Classify this cell by malaria status.
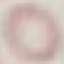
It is uninfected.

{
  "image_type": "cell patch, automatically extracted from a larger field of view and resized to 64 × 64 pixels",
  "stain": "Giemsa",
  "capture": "smartphone through the microscope eyepiece",
  "preparation": "thin smear"
}